Name the parasite shown.
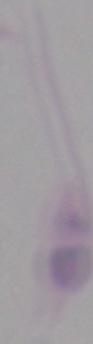

Leishmania.

Summary:
  - Modality: photomicrograph
  - Magnification: 1000x